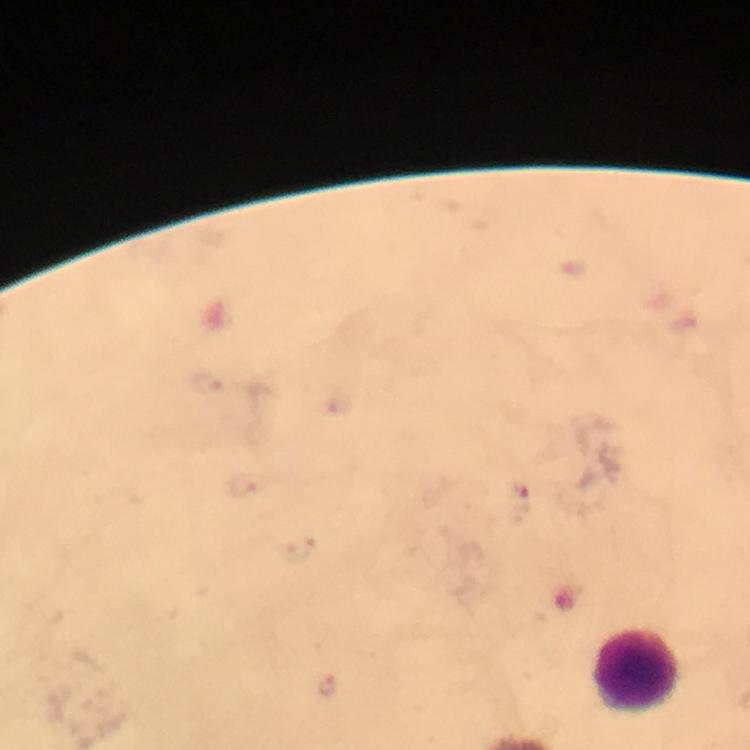
Approximate centers as {x, y} in pixels.
Summary:
  - Malaria parasite locations: {520, 500}, {326, 686}
  - Leukocyte locations: {637, 670}
  - Image size: 750×750 pixels
  - Stain: Giemsa
  - Magnification: 100x
  - Preparation: thick blood smear
  - Cropped from: one field of view
  - Immersion oil: used
  - Capture: smartphone mounted on the microscope
  - Context: from a diagnostic examination for malaria